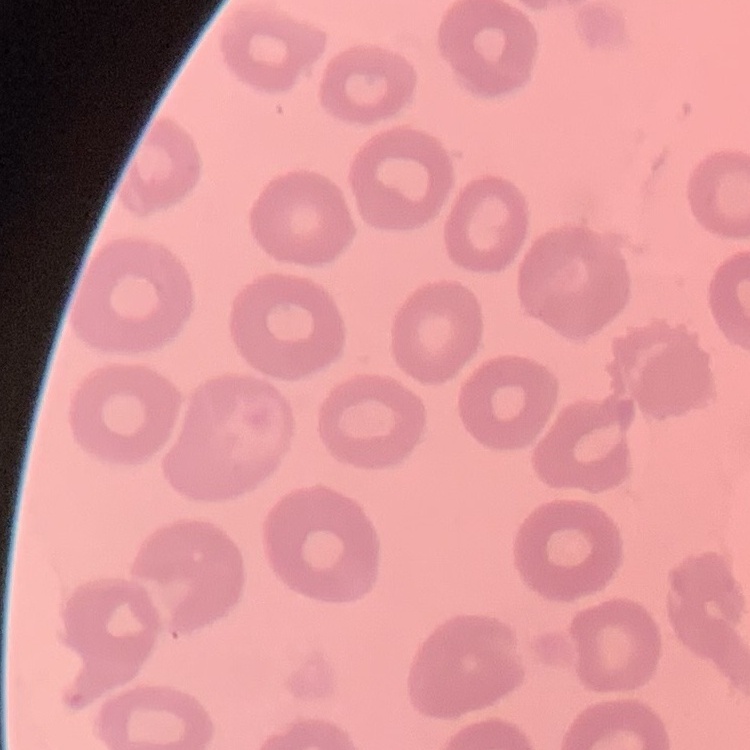

Summary:
  - Erythrocyte morphology: no rouleaux formation
  - Stain: Field's or Giemsa
  - Image type: one tile cut from a larger photomicrograph
  - Preparation: thin blood smear